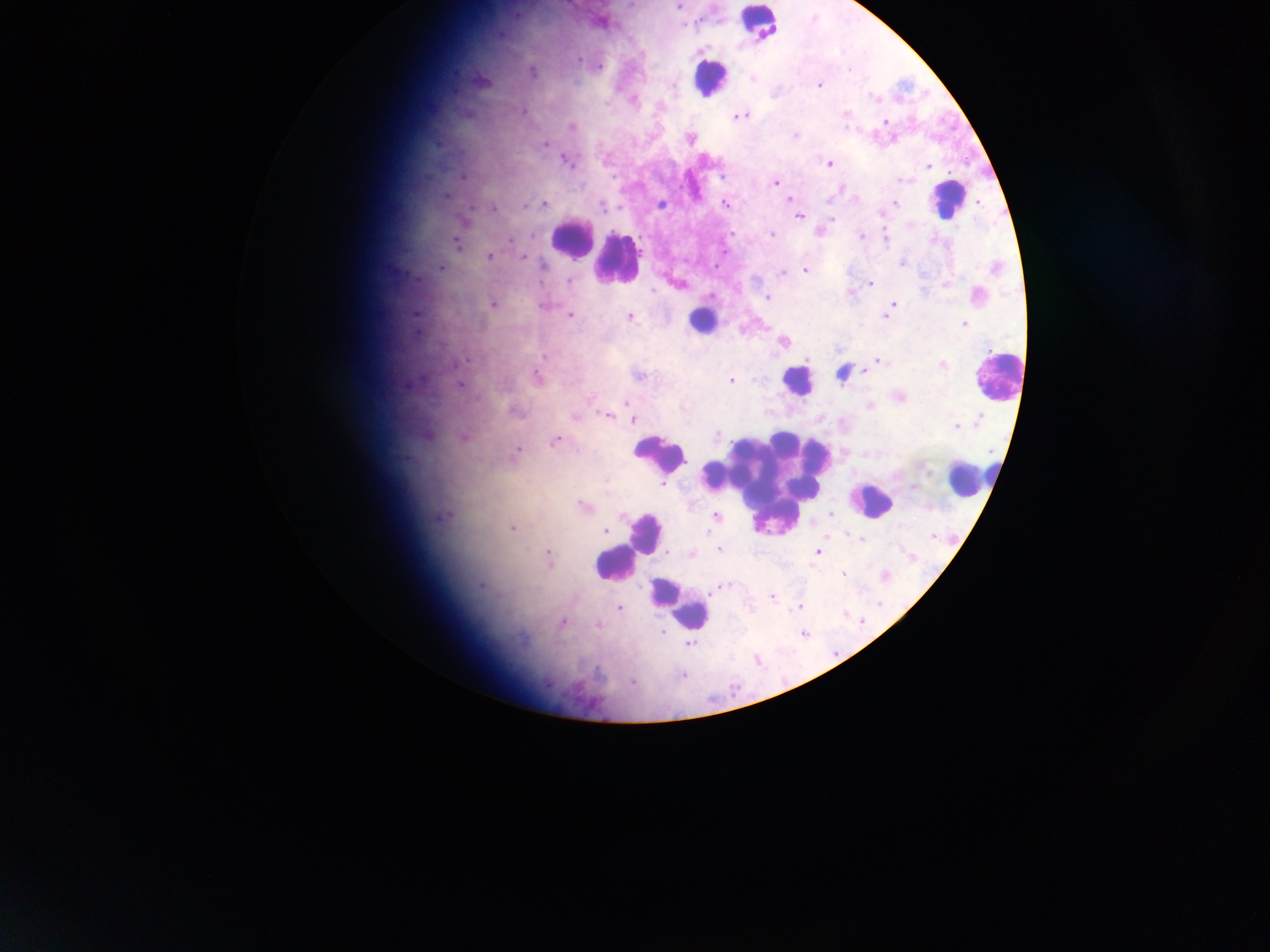

{
  "plasmodium_parasite_locations": "approximate centers as [x, y] in pixels: [679, 7], [534, 72], [753, 80], [820, 86], [608, 105], [848, 114], [741, 117], [886, 120], [572, 127], [796, 137], [691, 141], [546, 144], [566, 161], [830, 164], [929, 168], [777, 183], [844, 189], [791, 199], [544, 205], [897, 205], [662, 206], [727, 206], [526, 208], [603, 208], [493, 210], [800, 218], [822, 233], [732, 235], [773, 236], [862, 237], [511, 241], [888, 242], [458, 246], [524, 258], [490, 259], [904, 264], [544, 267], [442, 269], [806, 271], [784, 274], [570, 282], [871, 284], [769, 299], [494, 306], [545, 306], [894, 306], [891, 310], [417, 315], [571, 316], [630, 318], [888, 318], [966, 324], [785, 343], [546, 357], [467, 362], [880, 362], [943, 367], [845, 375], [640, 376], [539, 379], [732, 382], [460, 386], [629, 406], [871, 408], [514, 411], [577, 417], [608, 417], [634, 421], [979, 422], [958, 428], [716, 437], [466, 439], [557, 442], [518, 451], [664, 484], [584, 507], [832, 515], [717, 517], [623, 518], [513, 529], [605, 531], [936, 537], [860, 541], [720, 551], [818, 553], [693, 554], [550, 555], [913, 560], [843, 574], [887, 577], [723, 587], [481, 588], [774, 599], [880, 605], [800, 608], [620, 609], [847, 616], [862, 622], [563, 623], [600, 626], [664, 633], [805, 635], [690, 644], [759, 662], [684, 676]",
  "country": "Ghana",
  "preparation": "thick blood film",
  "capture": "mobile-phone photograph through a microscope",
  "leukocyte_locations": "approximate centers as [x, y] in pixels: [760, 25], [709, 80], [948, 201], [572, 241], [618, 259], [703, 321], [999, 379], [798, 383], [661, 455], [966, 481], [768, 488], [871, 502], [648, 533], [614, 564], [678, 603]",
  "image_size": "1270×952 pixels",
  "field_of_view": "single"
}